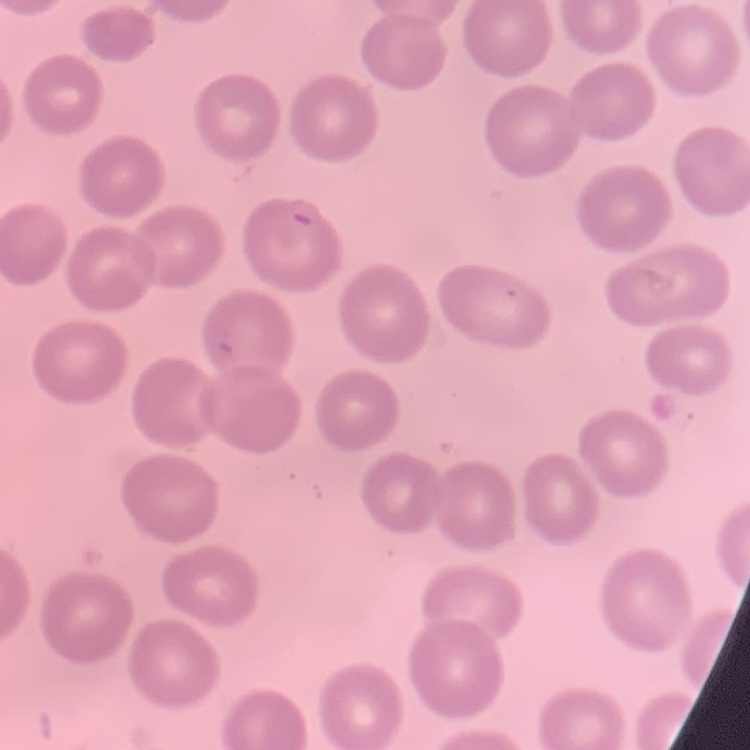

red_blood_cell_morphology: no rouleaux formation
stain: Field's or Giemsa
image_type: one tile cut from a larger photomicrograph
preparation: thin blood film